Locate and identify every blood parasite.
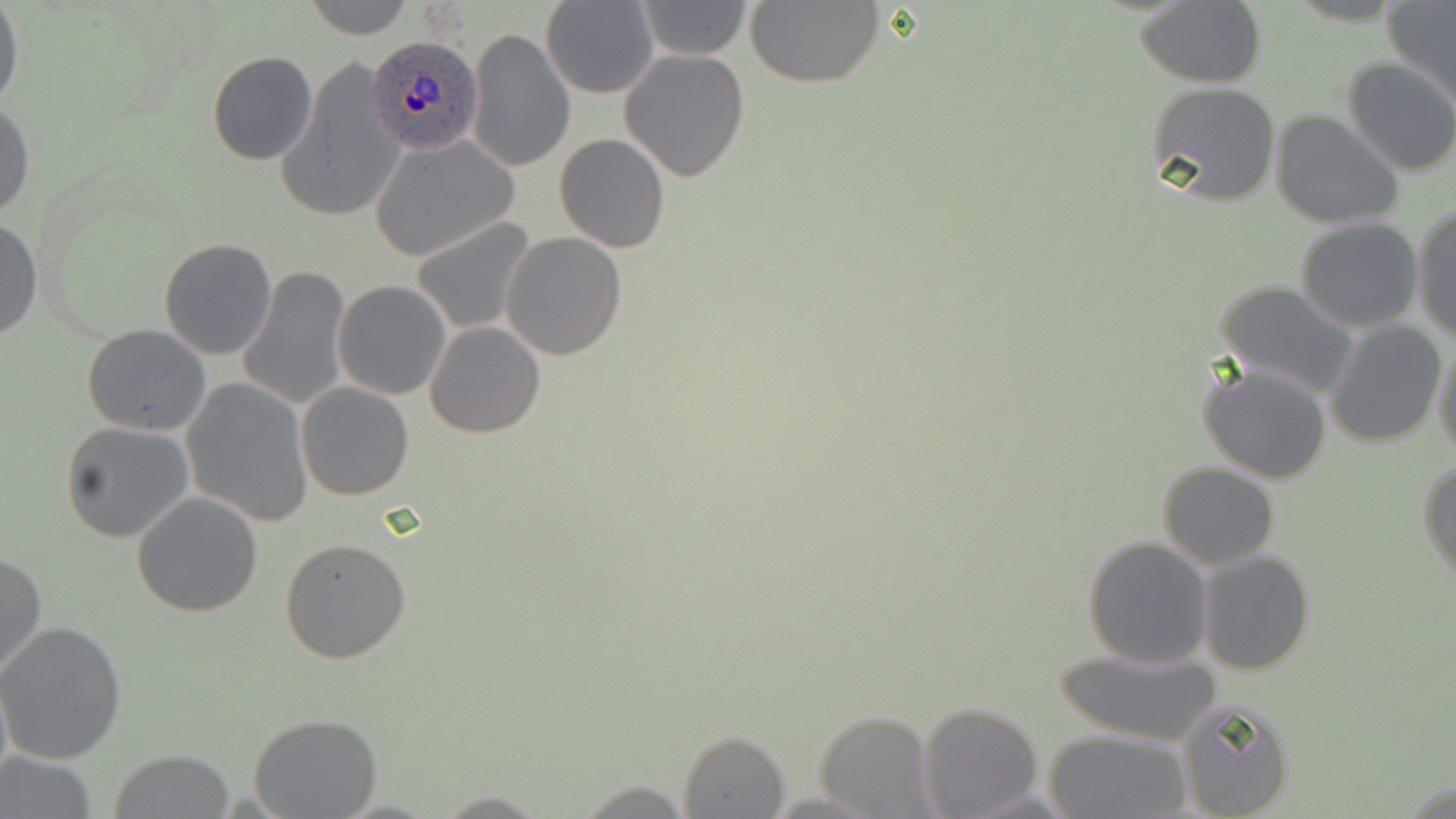
Approximate bounding boxes as named x1/y1/x2/y2 corners in pixels.
Plasmodium ovale-infected red blood cells: (x1=366, y1=33, x2=483, y2=156).
No Plasmodium falciparum, Plasmodium malariae, Plasmodium vivax, Babesia divergens, or Trypanosoma brucei observed.

{
  "slide_level_diagnosis": "Plasmodium ovale",
  "magnification": "1000x",
  "modality": "optical microscopy",
  "field_of_view": "single",
  "uninfected_red_blood_cell_locations": "approximate bounding boxes as named x1/y1/x2/y2 corners in pixels: (x1=301, y1=0, x2=416, y2=38), (x1=636, y1=0, x2=754, y2=59), (x1=539, y1=1, x2=660, y2=96), (x1=745, y1=1, x2=883, y2=88), (x1=1383, y1=1, x2=1456, y2=106), (x1=1133, y1=2, x2=1267, y2=87), (x1=0, y1=4, x2=23, y2=113), (x1=465, y1=27, x2=574, y2=171), (x1=619, y1=46, x2=750, y2=183), (x1=206, y1=51, x2=319, y2=165), (x1=274, y1=57, x2=406, y2=224), (x1=1343, y1=57, x2=1456, y2=176), (x1=1145, y1=82, x2=1282, y2=207), (x1=0, y1=101, x2=35, y2=224), (x1=1269, y1=109, x2=1404, y2=228), (x1=554, y1=133, x2=671, y2=254), (x1=369, y1=135, x2=518, y2=261), (x1=1411, y1=202, x2=1455, y2=343), (x1=0, y1=214, x2=42, y2=344), (x1=409, y1=217, x2=538, y2=335), (x1=1295, y1=219, x2=1423, y2=334), (x1=501, y1=231, x2=628, y2=359), (x1=157, y1=238, x2=277, y2=360), (x1=238, y1=265, x2=350, y2=412), (x1=334, y1=281, x2=453, y2=401), (x1=1214, y1=281, x2=1360, y2=400), (x1=1323, y1=319, x2=1446, y2=447), (x1=425, y1=322, x2=545, y2=438), (x1=82, y1=324, x2=212, y2=436), (x1=1431, y1=337, x2=1456, y2=462), (x1=1198, y1=362, x2=1332, y2=483), (x1=181, y1=377, x2=313, y2=527), (x1=297, y1=382, x2=414, y2=500), (x1=60, y1=421, x2=195, y2=542), (x1=1418, y1=458, x2=1456, y2=585), (x1=1157, y1=463, x2=1280, y2=571), (x1=132, y1=492, x2=262, y2=617), (x1=1083, y1=535, x2=1214, y2=668), (x1=281, y1=536, x2=411, y2=664), (x1=1199, y1=551, x2=1317, y2=675), (x1=0, y1=552, x2=47, y2=683), (x1=0, y1=620, x2=127, y2=764), (x1=1051, y1=645, x2=1225, y2=748), (x1=0, y1=667, x2=13, y2=794), (x1=1175, y1=697, x2=1295, y2=818), (x1=918, y1=701, x2=1043, y2=818), (x1=813, y1=711, x2=936, y2=819), (x1=248, y1=714, x2=383, y2=819), (x1=678, y1=729, x2=792, y2=819), (x1=1044, y1=730, x2=1191, y2=818), (x1=108, y1=750, x2=234, y2=818), (x1=1, y1=752, x2=100, y2=819), (x1=570, y1=779, x2=695, y2=816), (x1=431, y1=791, x2=554, y2=818)",
  "preparation": "thin blood smear",
  "image_size": "1456×819 pixels",
  "stain": "May-Grünwald-Giemsa"
}